Assess for malaria.
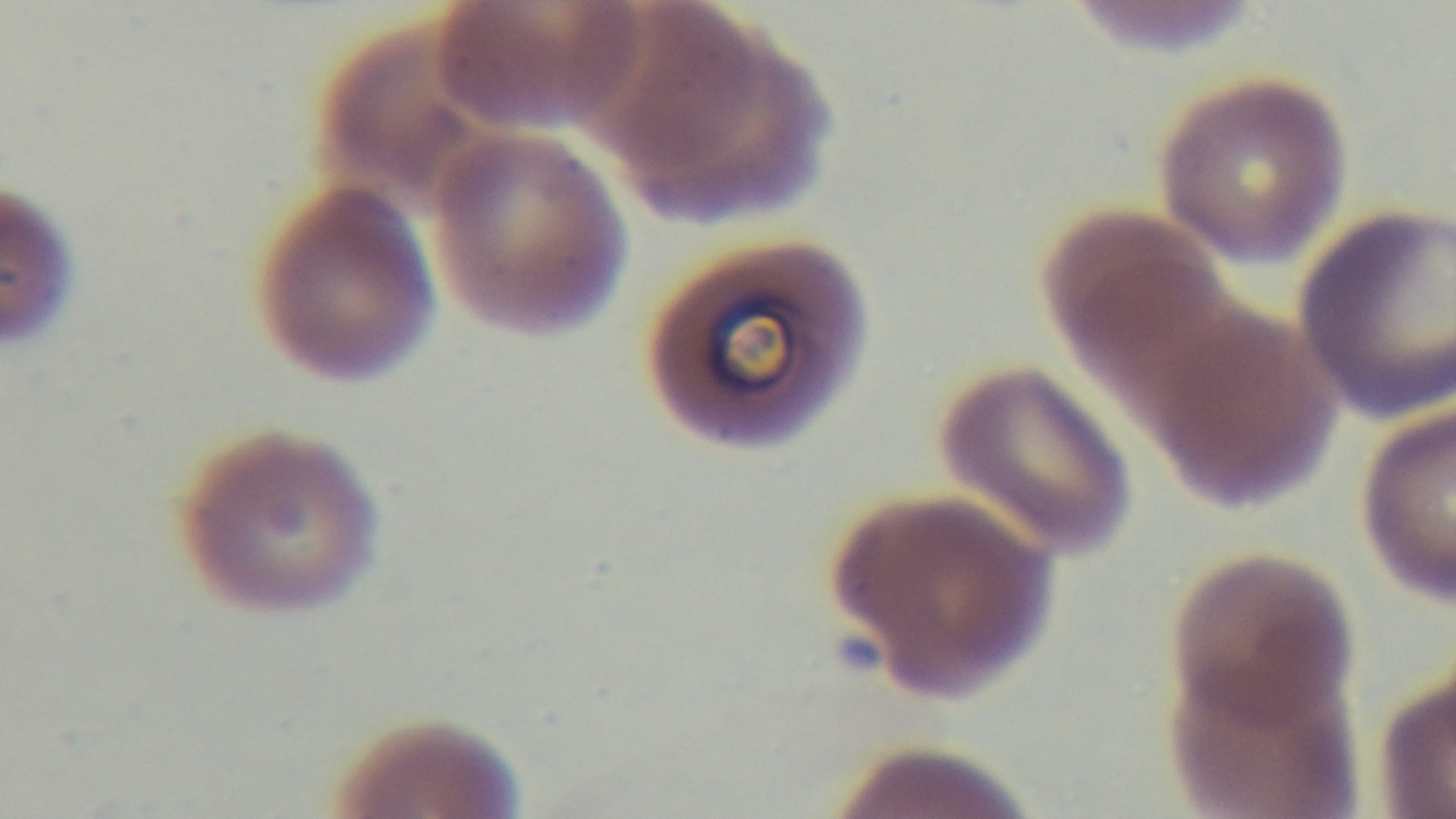

Infected.

Captured with a mounted 4K digital camera. Giemsa-stained. 100x oil-immersion objective. Preparation: thin smear. Single field of view. Light microscopy.